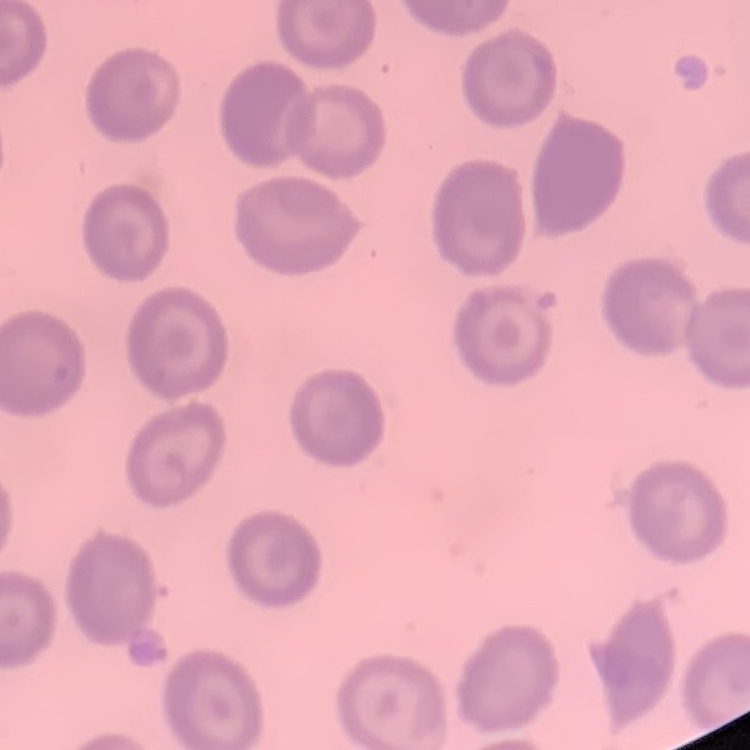

Summary:
  - Red blood cell morphology: no rouleaux formation
  - Image type: one tile cut from a larger photomicrograph
  - Stain: Field's or Giemsa
  - Preparation: thin peripheral smear